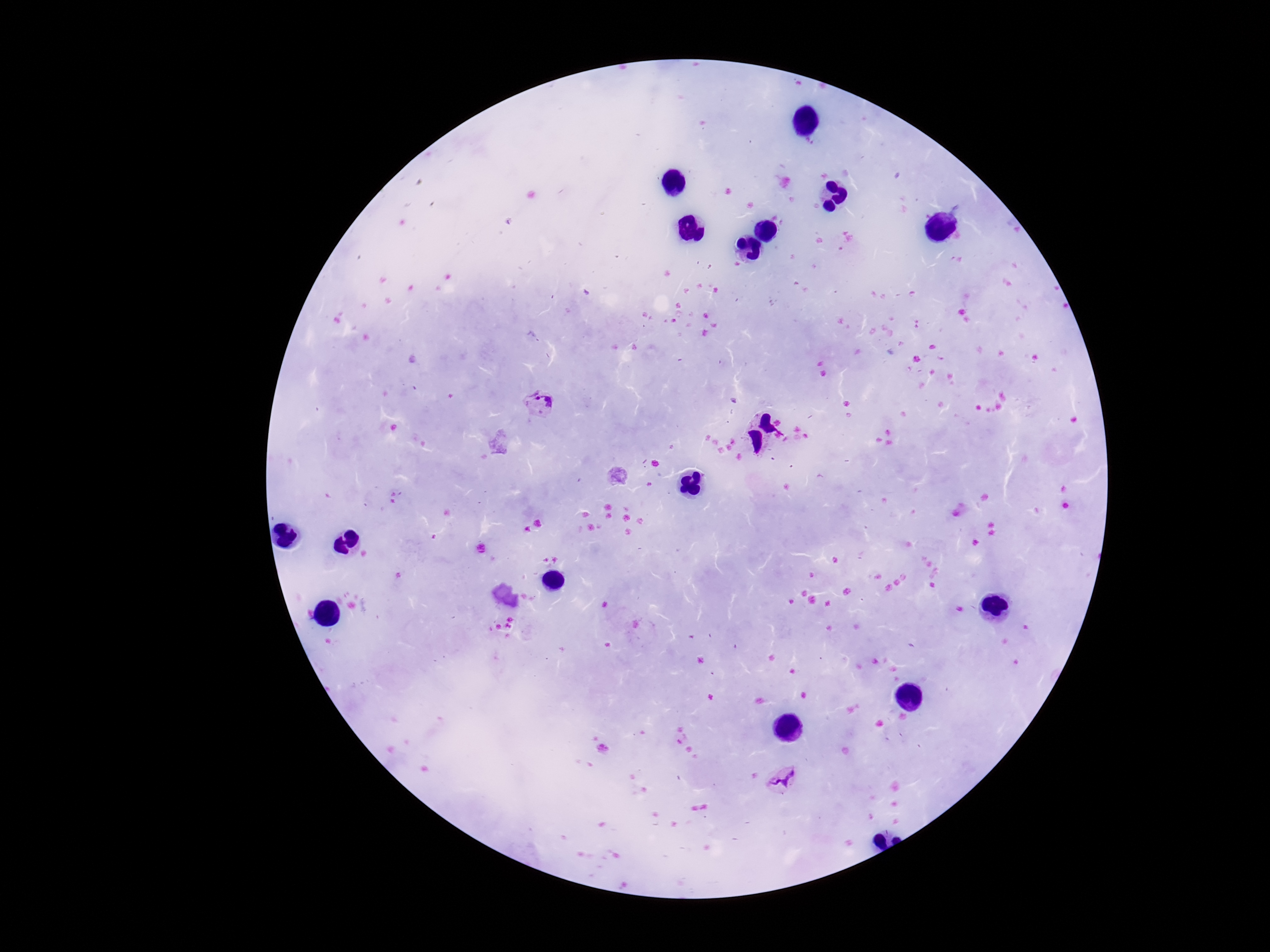

Approximate centers as (x, y) in pixels. Plasmodium parasite locations: (541, 405), (780, 778). Patient malaria status: positive. Photographed through the microscope eyepiece with a smartphone camera. Single field of view. Image is 1270×952 pixels. Thick blood smear. 100x magnification. Giemsa-stained preparation.